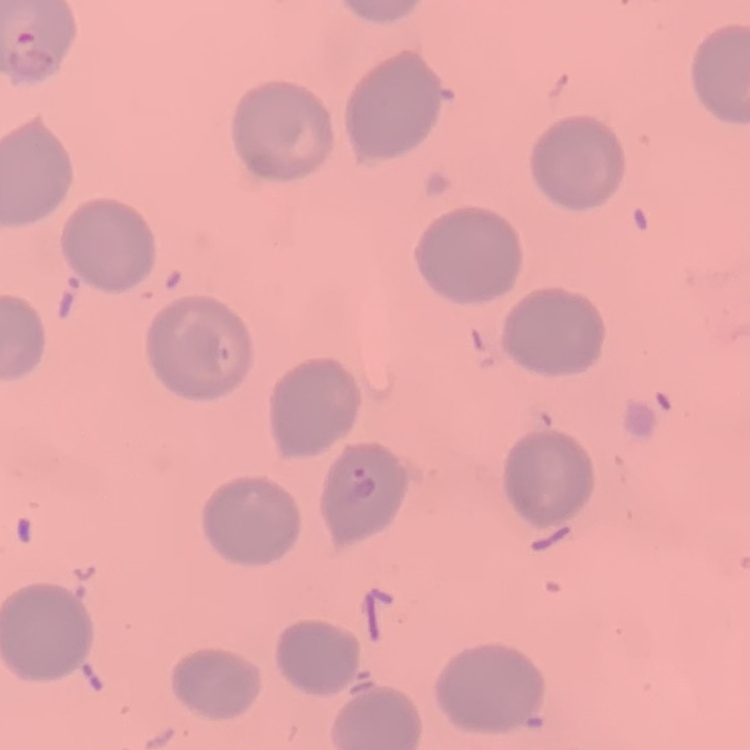
red_blood_cell_morphology: no rouleaux formation
stain: Field's or Giemsa
preparation: thin blood smear
image_type: square crop of a larger photomicrograph